Report the malaria status of this cell.
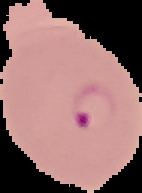

Parasitized.

Summary:
  - Preparation: thin blood smear
  - Image type: segmented cell region on a black background
  - Image size: 142×193 pixels